State the blood parasite species.
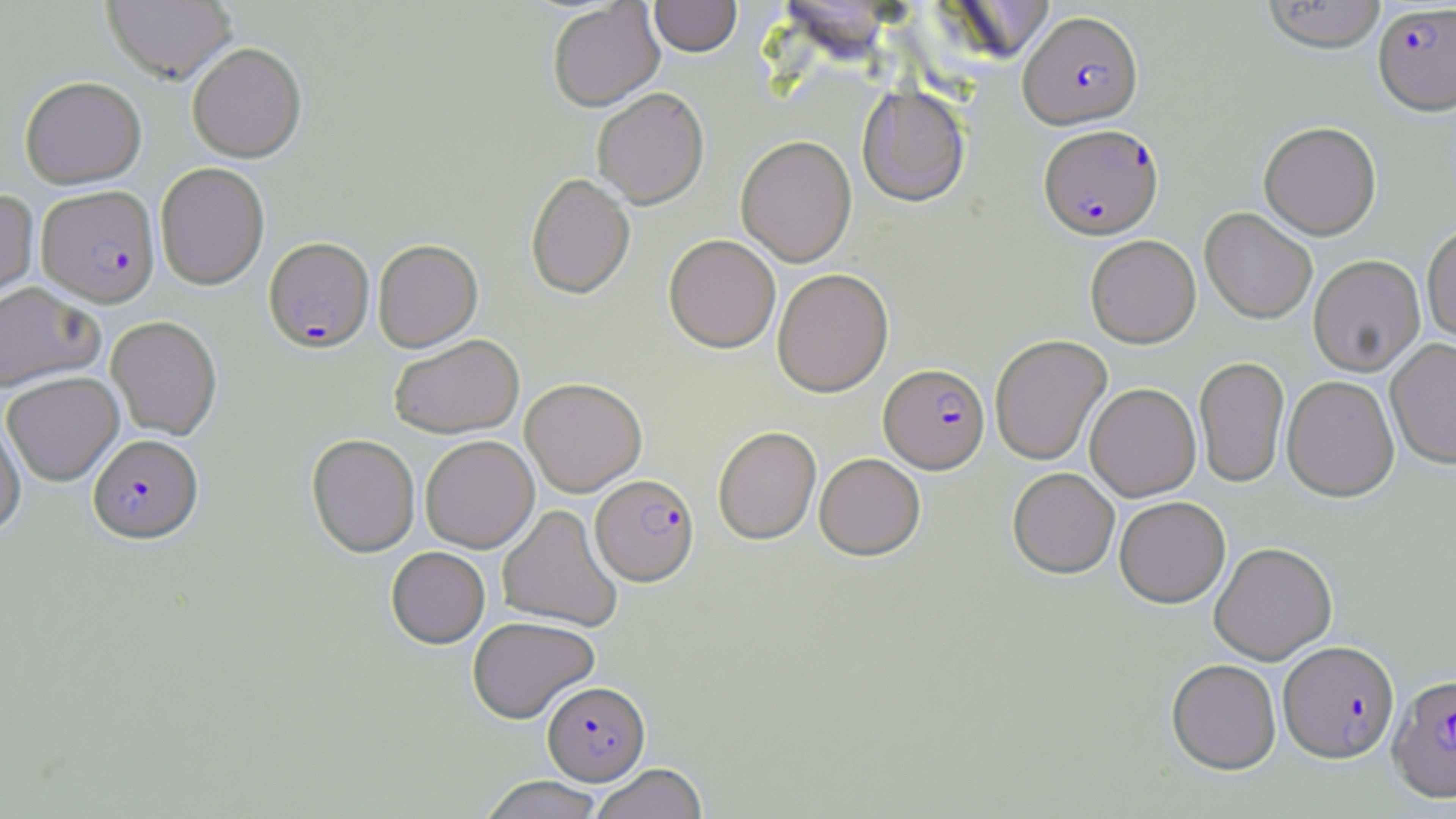
Plasmodium falciparum.

Approximate bounding boxes as (x1,y1)-(x2,y2) corner pairs in pixels. Plasmodium falciparum-infected red blood cell locations: (1373,3)-(1456,118), (1018,12)-(1143,132), (1038,125)-(1163,241), (37,185)-(160,307), (264,237)-(374,353), (880,364)-(990,474), (88,434)-(203,543), (590,475)-(699,586), (1279,642)-(1399,764), (1388,674)-(1456,803), (542,681)-(650,785). Uninfected red blood cell locations: (103,0)-(237,84), (649,0)-(741,59), (1262,0)-(1387,56), (548,2)-(664,112), (187,42)-(306,162), (20,76)-(146,188), (857,86)-(970,208), (592,88)-(709,209), (1259,124)-(1382,240), (736,136)-(857,268), (155,162)-(269,290), (525,173)-(635,300), (0,189)-(39,309), (1200,208)-(1318,324), (1422,223)-(1456,345), (663,235)-(781,354), (1085,236)-(1201,348), (373,239)-(483,352), (1309,256)-(1426,377), (772,268)-(893,397), (0,282)-(104,392), (106,315)-(222,440), (389,334)-(523,439), (990,334)-(1112,465), (1386,339)-(1456,470), (1194,357)-(1290,487), (2,371)-(124,486), (1282,376)-(1400,502), (520,377)-(647,496), (1085,383)-(1201,501), (0,415)-(27,538), (713,426)-(821,545), (307,434)-(420,557), (420,435)-(539,552), (815,453)-(925,560), (1007,468)-(1119,578), (1115,496)-(1231,608), (497,505)-(622,632), (1209,543)-(1337,665), (386,547)-(490,648), (468,616)-(600,724), (1167,661)-(1281,776), (590,763)-(708,819), (479,775)-(604,819). 1000x magnification. May-Grünwald-Giemsa stain. Image is 1456×819 pixels. Single field of view. Light microscopy. Thin blood smear.